Locate every blood parasite and identify its species.
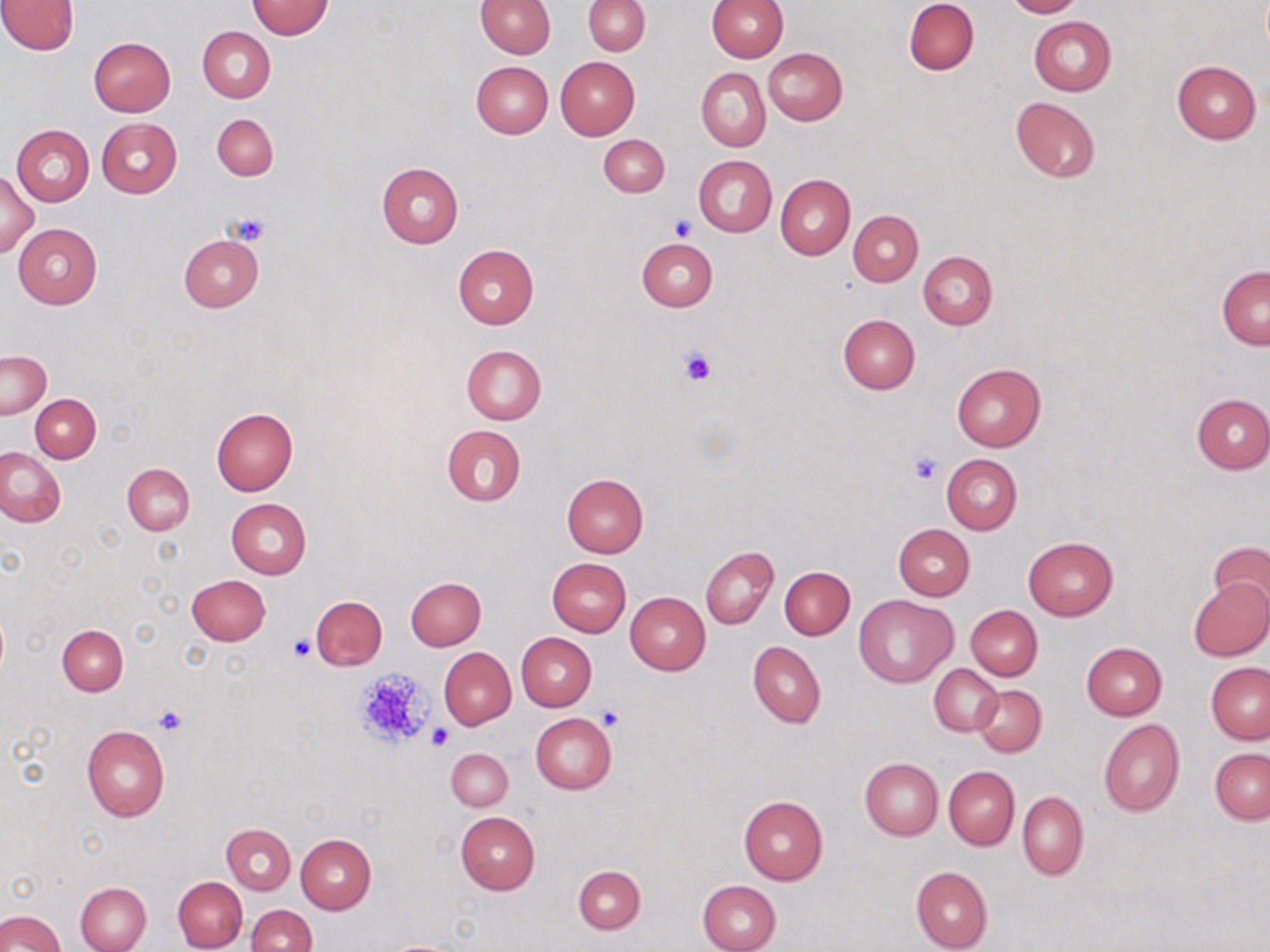

No blood parasites observed.

Approximate bounding boxes as [x1, y1, x2, y2] in pixels. Platelet locations: [227, 213, 272, 246], [669, 215, 698, 240], [676, 346, 718, 387], [908, 453, 942, 485], [287, 633, 317, 662], [351, 667, 437, 752], [151, 705, 189, 737], [596, 705, 625, 730], [428, 726, 454, 750]. Uninfected red blood cell locations: [0, 0, 78, 54], [477, 0, 555, 57], [583, 0, 650, 55], [708, 0, 788, 61], [904, 0, 979, 75], [1003, 0, 1082, 17], [246, 1, 333, 39], [1028, 16, 1117, 96], [198, 26, 275, 102], [88, 36, 176, 116], [762, 48, 847, 125], [556, 56, 640, 140], [1171, 59, 1261, 144], [471, 61, 552, 139], [696, 68, 770, 151], [1010, 97, 1101, 182], [211, 114, 278, 181], [96, 118, 182, 197], [12, 124, 94, 207], [598, 134, 669, 197], [693, 154, 776, 237], [376, 162, 463, 249], [0, 168, 38, 258], [775, 174, 854, 259], [848, 210, 923, 285], [14, 222, 102, 309], [178, 236, 264, 312], [637, 238, 717, 312], [453, 244, 539, 328], [918, 251, 997, 330], [1216, 266, 1269, 351], [837, 314, 919, 395], [461, 344, 546, 425], [1, 350, 51, 420], [951, 363, 1047, 451], [1191, 392, 1270, 474], [31, 394, 100, 462], [210, 407, 299, 496], [441, 425, 526, 506], [0, 447, 65, 527], [941, 454, 1021, 534], [123, 463, 195, 535], [562, 473, 649, 558], [226, 498, 312, 578], [893, 524, 974, 600], [1022, 535, 1119, 621], [1209, 541, 1270, 614], [701, 546, 778, 630], [548, 558, 631, 637], [780, 566, 855, 639], [186, 573, 271, 646], [406, 577, 486, 650], [1187, 577, 1270, 661], [625, 591, 710, 674], [855, 593, 958, 688], [311, 595, 387, 669], [965, 605, 1043, 681], [57, 625, 128, 695], [516, 632, 597, 711], [1081, 641, 1167, 720], [748, 642, 826, 729], [439, 647, 516, 729], [1206, 662, 1270, 744], [929, 664, 1002, 736], [973, 685, 1047, 756], [531, 714, 617, 794], [1098, 717, 1185, 816], [81, 725, 170, 822], [446, 748, 513, 810], [1210, 748, 1269, 823], [859, 758, 942, 840], [943, 766, 1019, 850], [1017, 791, 1088, 880], [738, 793, 827, 885], [455, 811, 540, 894], [222, 823, 295, 895], [296, 834, 376, 914], [573, 865, 645, 934], [909, 867, 992, 952], [173, 876, 248, 951], [697, 879, 781, 952], [76, 882, 152, 952], [247, 905, 317, 952], [0, 910, 65, 952], [380, 938, 470, 951]. Slide-level diagnosis: negative for blood parasites. Image is 1270×952 pixels. Thin blood smear. Single field of view. Optical microscopy. May-Grünwald-Giemsa-stained preparation. Captured at 1000x magnification.